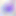
modality = micrograph
magnification = 400x
identification = Toxoplasma gondii